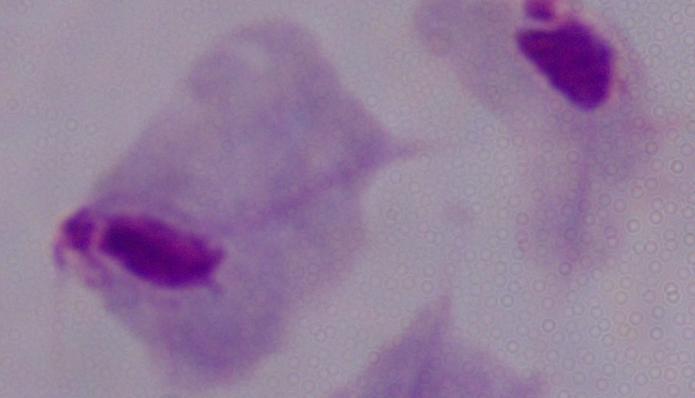
Summary:
  - Identification: trichomonad
  - Magnification: 1000x
  - Modality: micrograph